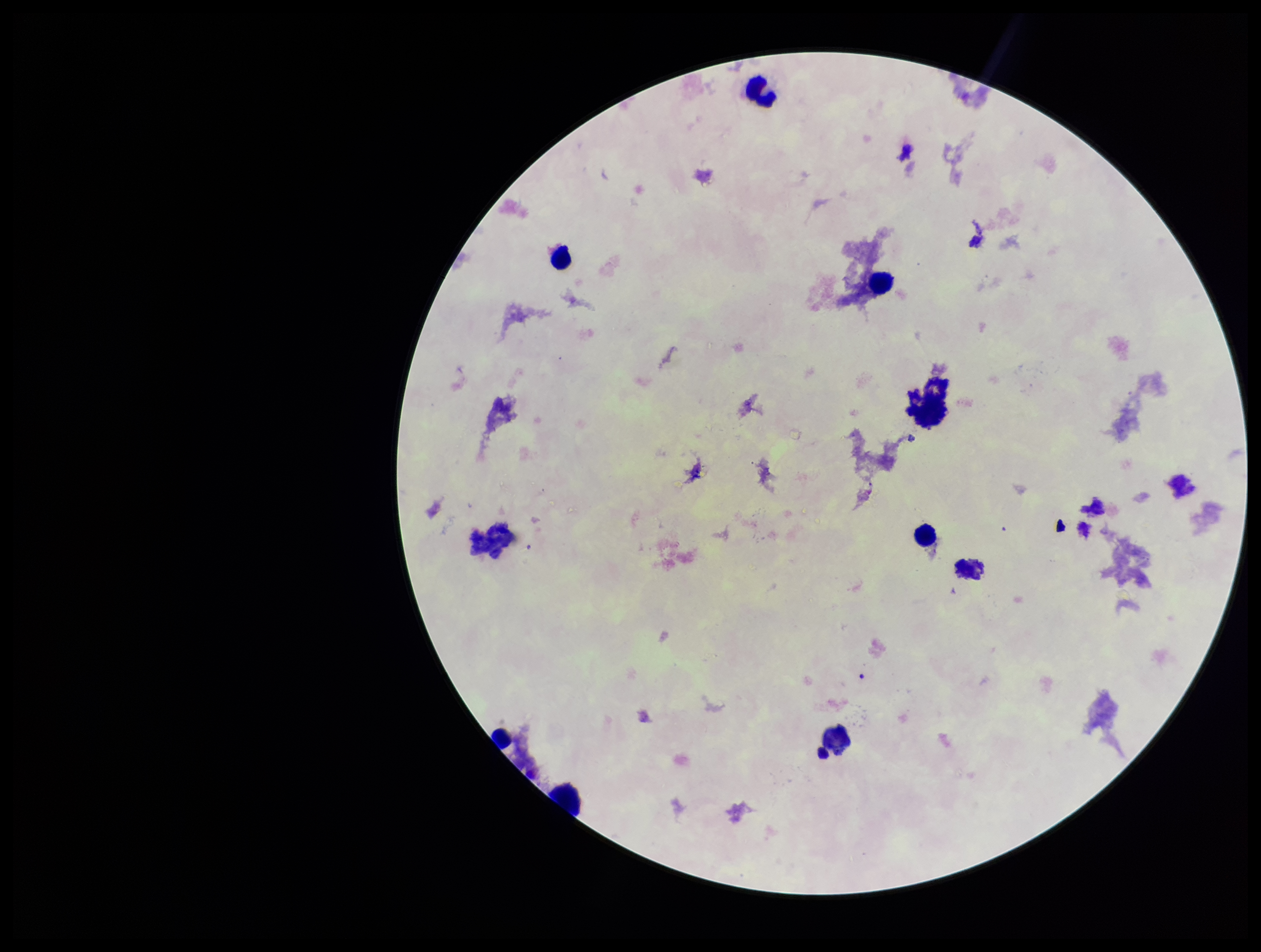

plasmodium_parasites: none identified
preparation: thick
patient_malaria_status: negative
stain: Giemsa
capture: smartphone photograph through the microscope eyepiece
image_size: 1261×952 pixels
parasite_count: 0
field_of_view: one from this slide
leukocyte_count: 10